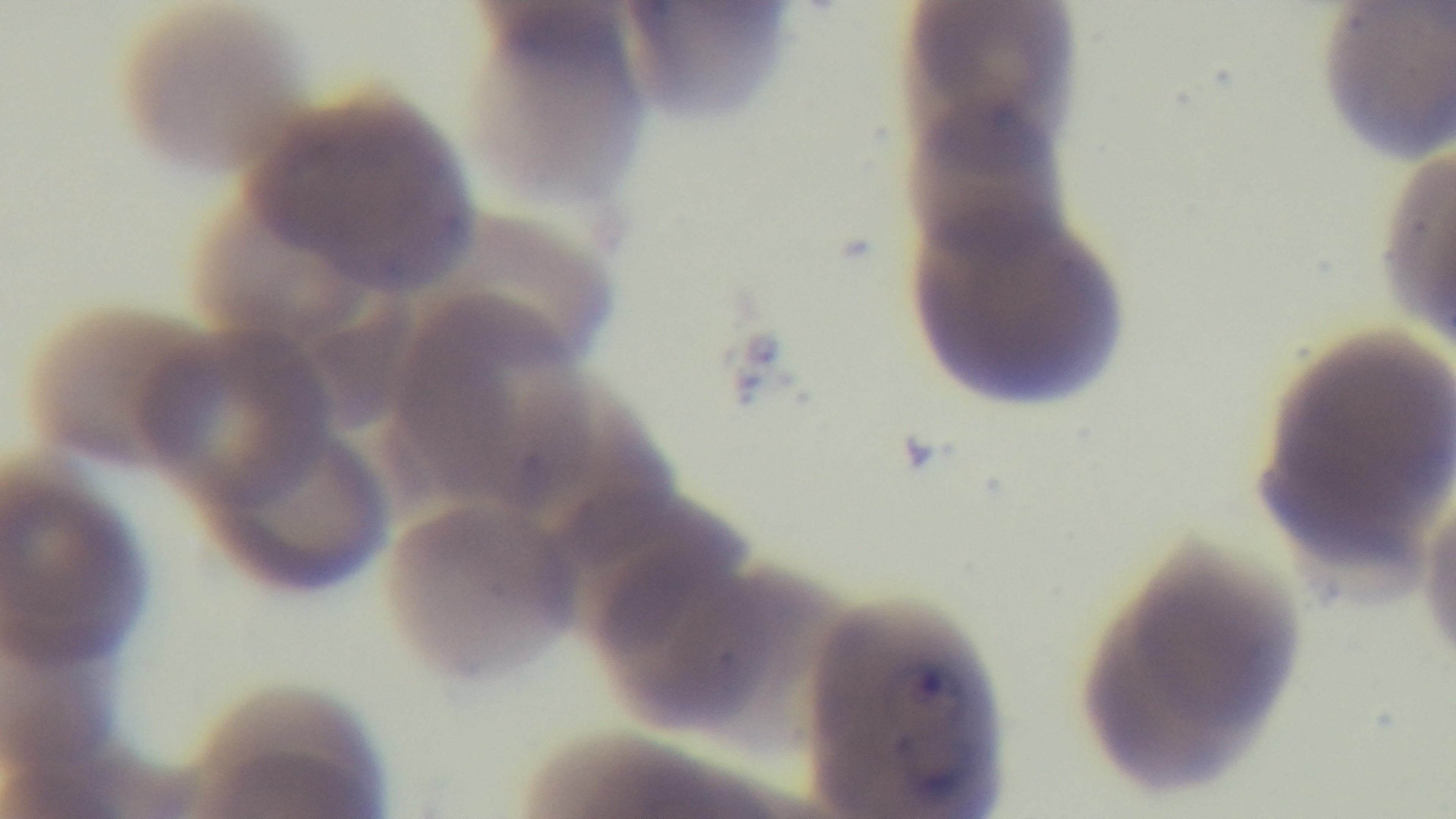
Captured with a mounted 4K digital camera. 100x oil-immersion objective. Giemsa stain. Malaria status: positive. One field from the slide. Preparation: thin smear. Photomicrograph.